Report the malaria status of this cell.
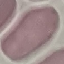

It is uninfected.

Summary:
  - Preparation: thin blood film
  - Stain: Giemsa
  - Image type: cell patch, automatically extracted from a larger field of view and resized to 64 × 64 pixels
  - Capture: smartphone through the microscope eyepiece